Identify the parasite.
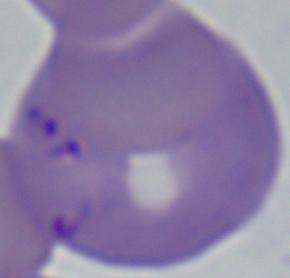

Babesia.

{
  "magnification": "1000x",
  "modality": "photomicrograph"
}